Report the malaria status of this cell.
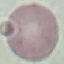
Uninfected.

Photographed with a smartphone camera at the microscope eyepiece. Giemsa-stained preparation. Cell patch, automatically extracted from a larger field of view and resized to 64 × 64 pixels. Thin blood film.